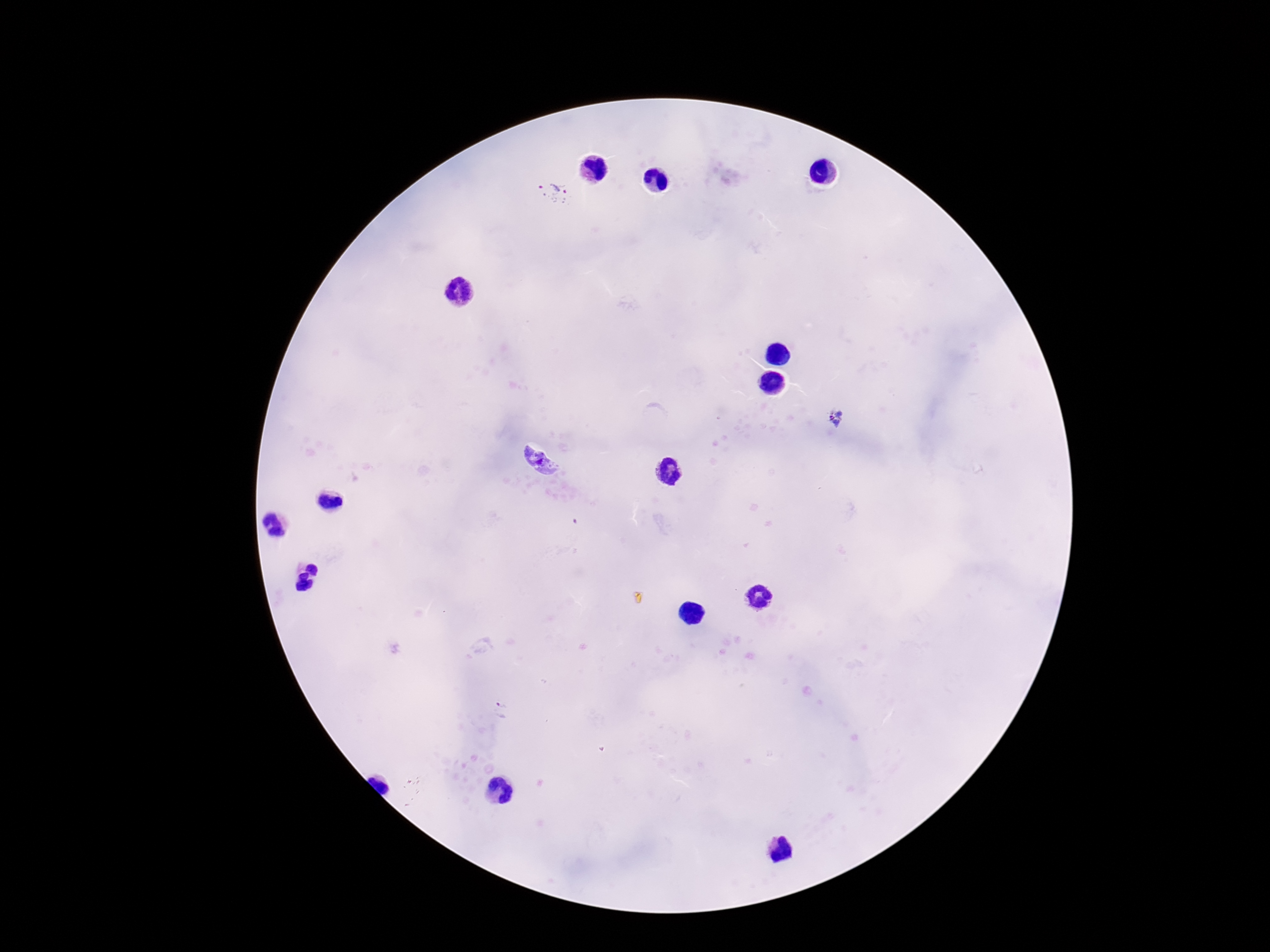

{
  "magnification": "100x",
  "stain": "Giemsa",
  "plasmodium_parasite_locations": "approximate object centers, in pixels from the top-left corner: (x=556, y=191), (x=837, y=418), (x=541, y=463)",
  "preparation": "thick peripheral-blood smear",
  "patient_malaria_status": "infected",
  "field_of_view": "one from this slide",
  "capture": "smartphone camera through the microscope eyepiece",
  "image_size": "1270×952 pixels"
}